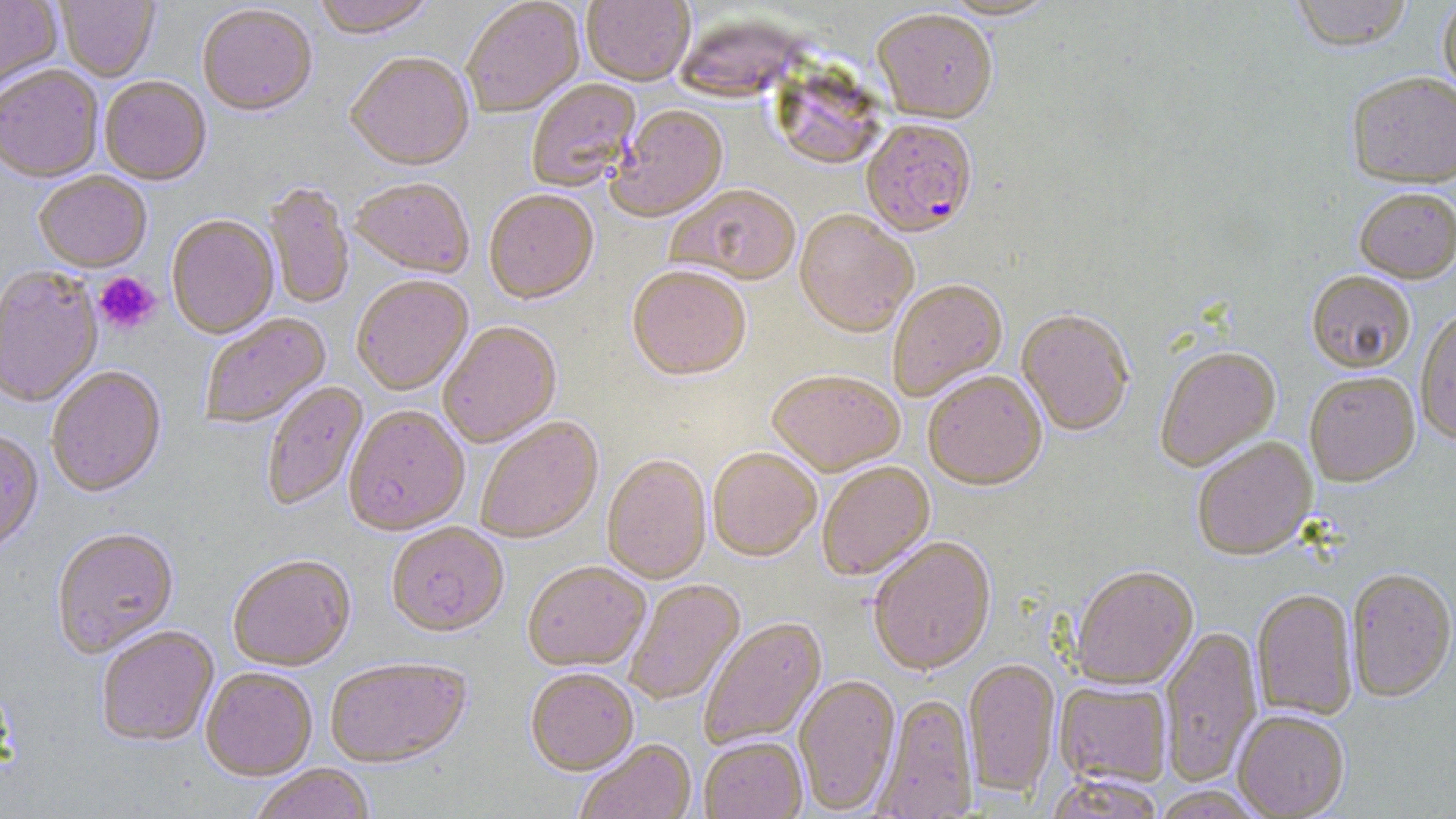
Approximate bounding boxes as named x1/y1/x2/y2 corners in pixels. Platelet locations: (x1=95, y1=272, x2=160, y2=333). Uninfected red blood cell locations: (x1=0, y1=0, x2=63, y2=95), (x1=55, y1=0, x2=160, y2=84), (x1=312, y1=0, x2=437, y2=42), (x1=582, y1=0, x2=695, y2=88), (x1=939, y1=0, x2=1062, y2=23), (x1=1290, y1=0, x2=1414, y2=53), (x1=1437, y1=0, x2=1456, y2=103), (x1=462, y1=1, x2=585, y2=119), (x1=198, y1=6, x2=317, y2=120), (x1=872, y1=12, x2=998, y2=126), (x1=672, y1=21, x2=807, y2=101), (x1=346, y1=55, x2=475, y2=173), (x1=778, y1=59, x2=886, y2=166), (x1=0, y1=67, x2=103, y2=186), (x1=1346, y1=72, x2=1456, y2=190), (x1=99, y1=78, x2=211, y2=187), (x1=527, y1=79, x2=643, y2=194), (x1=609, y1=106, x2=728, y2=224), (x1=34, y1=173, x2=152, y2=274), (x1=350, y1=180, x2=473, y2=280), (x1=265, y1=183, x2=354, y2=311), (x1=668, y1=186, x2=801, y2=287), (x1=1354, y1=189, x2=1456, y2=284), (x1=484, y1=192, x2=599, y2=306), (x1=794, y1=212, x2=917, y2=339), (x1=167, y1=216, x2=279, y2=341), (x1=0, y1=268, x2=103, y2=409), (x1=627, y1=268, x2=751, y2=383), (x1=1306, y1=273, x2=1414, y2=374), (x1=352, y1=277, x2=473, y2=397), (x1=888, y1=281, x2=1008, y2=402), (x1=1415, y1=309, x2=1456, y2=445), (x1=1016, y1=312, x2=1134, y2=438), (x1=200, y1=313, x2=333, y2=430), (x1=439, y1=323, x2=562, y2=449), (x1=1156, y1=349, x2=1281, y2=473), (x1=47, y1=368, x2=166, y2=499), (x1=766, y1=372, x2=905, y2=479), (x1=923, y1=374, x2=1047, y2=492), (x1=1304, y1=374, x2=1420, y2=487), (x1=262, y1=382, x2=369, y2=512), (x1=344, y1=407, x2=470, y2=538), (x1=476, y1=418, x2=604, y2=545), (x1=0, y1=432, x2=44, y2=557), (x1=1192, y1=439, x2=1318, y2=562), (x1=708, y1=449, x2=822, y2=563), (x1=602, y1=456, x2=711, y2=586), (x1=817, y1=462, x2=935, y2=582), (x1=387, y1=524, x2=509, y2=639), (x1=51, y1=529, x2=179, y2=659), (x1=868, y1=538, x2=997, y2=678), (x1=228, y1=557, x2=355, y2=672), (x1=523, y1=563, x2=651, y2=673), (x1=1070, y1=567, x2=1198, y2=691), (x1=1347, y1=570, x2=1456, y2=703), (x1=625, y1=580, x2=745, y2=706), (x1=1251, y1=590, x2=1357, y2=721), (x1=699, y1=618, x2=828, y2=751), (x1=1160, y1=625, x2=1262, y2=786), (x1=96, y1=628, x2=219, y2=748), (x1=963, y1=659, x2=1061, y2=799), (x1=325, y1=660, x2=472, y2=770), (x1=200, y1=669, x2=317, y2=782), (x1=526, y1=670, x2=639, y2=778), (x1=793, y1=675, x2=900, y2=815), (x1=1053, y1=680, x2=1172, y2=789), (x1=872, y1=695, x2=978, y2=819), (x1=1232, y1=711, x2=1349, y2=819), (x1=699, y1=738, x2=807, y2=819), (x1=575, y1=740, x2=697, y2=819), (x1=250, y1=766, x2=375, y2=819), (x1=1045, y1=773, x2=1165, y2=819), (x1=1150, y1=787, x2=1263, y2=818). Plasmodium falciparum-infected red blood cell locations: (x1=860, y1=121, x2=978, y2=241). Slide-level diagnosis: Plasmodium falciparum. Thin blood smear. May-Grünwald-Giemsa-stained preparation. Optical microscopy. Captured at 1000x magnification. Image is 1456×819 pixels. Single field of view.